Point out every malaria parasite.
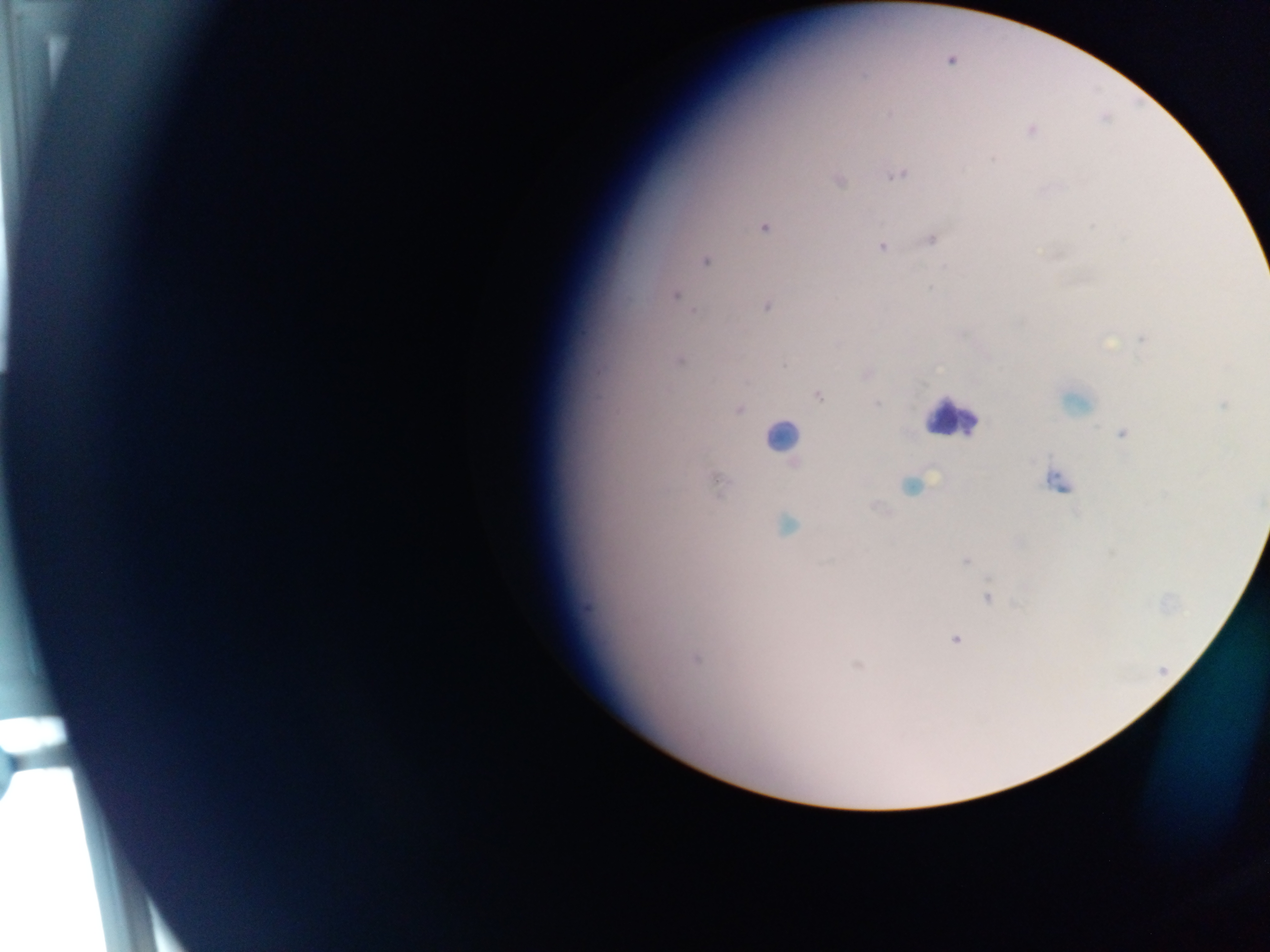

Approximate centers as x y in pixels.
Malaria parasites: 1031 130; 994 159; 897 175; 838 181; 764 228; 932 239; 882 247; 705 261; 930 287; 675 294; 767 306; 1143 339; 1109 343; 785 365; 866 374; 818 396; 877 404; 1224 405; 740 410; 1122 434; 795 464; 1056 481; 716 483; 911 486; 878 507; 787 525; 965 561; 987 597; 956 639; 696 659; 858 666.
One object is labeled both malaria parasite and leukocyte by the source: 1075 401.

image size = 1270×952 pixels
capture = mobile-phone photograph through a microscope
field of view = single
preparation = thick blood smear
country = Ghana
leukocyte locations = approximate centers as x y in pixels: 952 418; 781 436